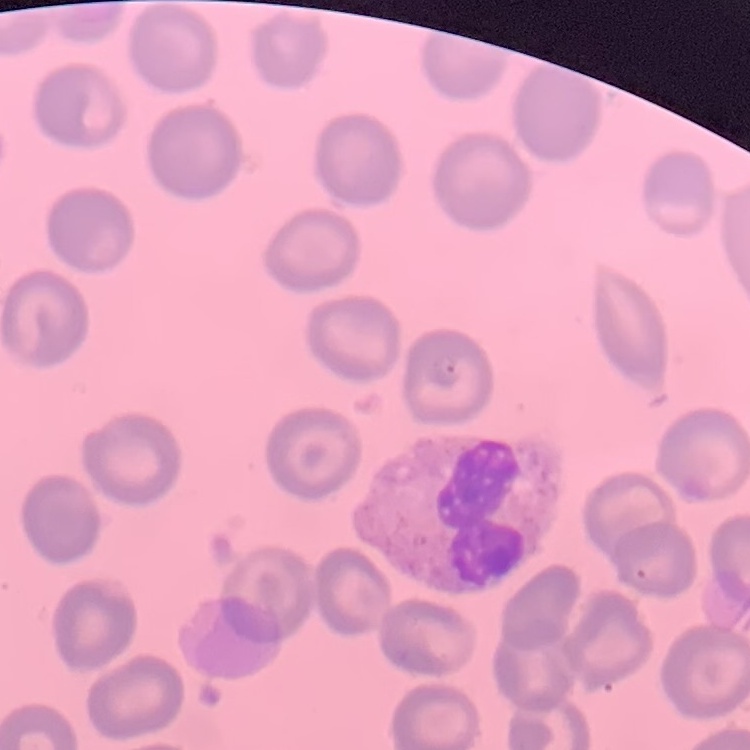

red blood cell morphology = no rouleaux formation
image type = one tile cut from a larger photomicrograph
stain = Field's or Giemsa
preparation = thin blood film